Assess this cell for malaria.
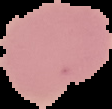

Uninfected.

image size = 112×109 pixels
preparation = thin blood film
image type = cell region segmented out of the field of view; surrounding area masked to black